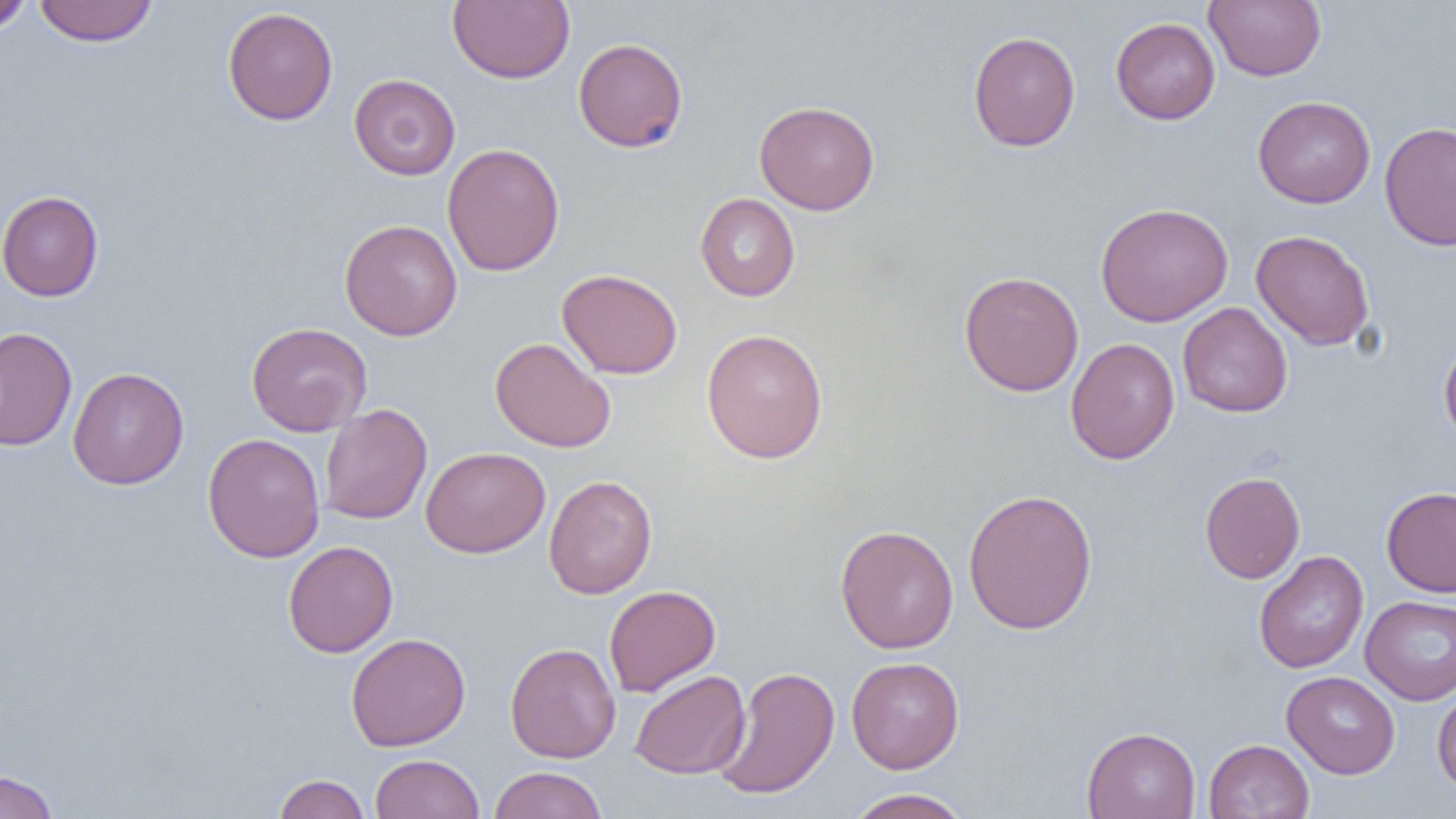

slide-level diagnosis = no evidence of blood parasites
uninfected red blood cell locations = approximate bounding boxes as named x1/y1/x2/y2 corners in pixels: (x1=0, y1=0, x2=33, y2=36), (x1=33, y1=0, x2=158, y2=47), (x1=447, y1=0, x2=574, y2=84), (x1=1204, y1=0, x2=1326, y2=81), (x1=223, y1=7, x2=338, y2=125), (x1=1111, y1=17, x2=1220, y2=125), (x1=967, y1=30, x2=1081, y2=152), (x1=573, y1=37, x2=689, y2=153), (x1=349, y1=74, x2=461, y2=180), (x1=1252, y1=96, x2=1375, y2=208), (x1=754, y1=100, x2=880, y2=215), (x1=1379, y1=122, x2=1456, y2=251), (x1=442, y1=143, x2=565, y2=276), (x1=0, y1=190, x2=104, y2=301), (x1=695, y1=193, x2=800, y2=301), (x1=1095, y1=202, x2=1233, y2=326), (x1=339, y1=219, x2=463, y2=341), (x1=1250, y1=230, x2=1376, y2=351), (x1=556, y1=268, x2=683, y2=379), (x1=958, y1=271, x2=1084, y2=397), (x1=1178, y1=302, x2=1292, y2=417), (x1=246, y1=321, x2=372, y2=436), (x1=0, y1=326, x2=77, y2=451), (x1=701, y1=328, x2=828, y2=463), (x1=489, y1=337, x2=617, y2=453), (x1=1065, y1=337, x2=1179, y2=465), (x1=1439, y1=337, x2=1456, y2=449), (x1=67, y1=367, x2=189, y2=490), (x1=319, y1=404, x2=432, y2=525), (x1=202, y1=432, x2=325, y2=563), (x1=421, y1=446, x2=550, y2=558), (x1=1199, y1=471, x2=1305, y2=583), (x1=544, y1=474, x2=657, y2=599), (x1=1381, y1=486, x2=1456, y2=598), (x1=962, y1=488, x2=1098, y2=635), (x1=835, y1=524, x2=959, y2=654), (x1=283, y1=540, x2=398, y2=658), (x1=1253, y1=550, x2=1369, y2=674), (x1=604, y1=584, x2=721, y2=697), (x1=1360, y1=595, x2=1456, y2=704), (x1=345, y1=632, x2=471, y2=751), (x1=505, y1=642, x2=621, y2=763), (x1=847, y1=656, x2=965, y2=773), (x1=714, y1=665, x2=839, y2=799), (x1=630, y1=669, x2=750, y2=779), (x1=1281, y1=671, x2=1401, y2=779), (x1=1432, y1=682, x2=1456, y2=796), (x1=1081, y1=726, x2=1200, y2=819), (x1=1203, y1=739, x2=1314, y2=819), (x1=370, y1=753, x2=484, y2=819), (x1=489, y1=766, x2=608, y2=819), (x1=0, y1=769, x2=58, y2=819), (x1=273, y1=774, x2=370, y2=819), (x1=845, y1=789, x2=972, y2=818)
magnification = 1000x
preparation = thin blood smear
field of view = one of a larger specimen
modality = light microscopy
image size = 1456×819 pixels